Assess this cell for malaria.
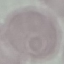
Uninfected.

Giemsa-stained preparation. Acquired by smartphone through the microscope eyepiece. Automatically extracted cell patch, resized to 64 × 64 pixels. Thin smear of blood.